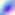

identification = Toxoplasma gondii
magnification = 400x
modality = photomicrograph